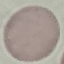

Summary:
  - Result: negative for malaria parasites
  - Image type: automatically extracted cell patch, resized to 64 × 64 pixels
  - Capture: smartphone camera at the microscope eyepiece
  - Stain: Giemsa
  - Preparation: thin blood film